Locate every Plasmodium falciparum-infected red blood cell.
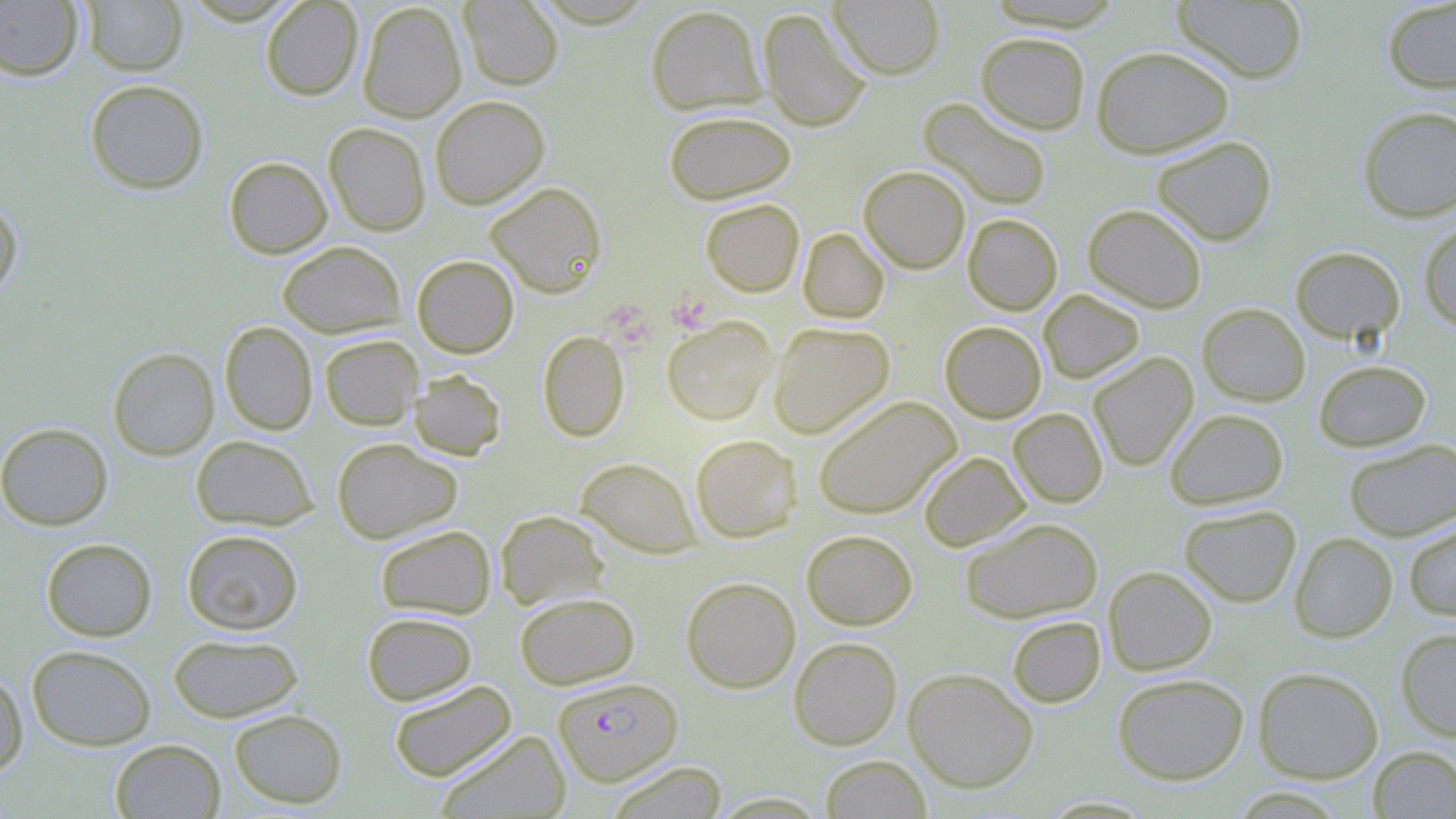
Approximate bounding boxes as (x1, y1, x2, y2) in pixels.
Plasmodium falciparum-infected red blood cells: (552, 677, 683, 786).

slide-level diagnosis = Plasmodium falciparum
preparation = thin blood film
magnification = 1000x
modality = light microscopy
stain = May-Grünwald-Giemsa
field of view = one of a larger specimen
platelet locations = approximate bounding boxes as (x1, y1, x2, y2) in pixels: (670, 296, 712, 336), (599, 302, 657, 363)
image size = 1456×819 pixels
uninfected red blood cell locations = approximate bounding boxes as (x1, y1, x2, y2) in pixels: (80, 0, 187, 75), (260, 0, 364, 101), (458, 0, 564, 90), (828, 0, 946, 80), (1172, 0, 1309, 83), (0, 1, 83, 80), (1381, 1, 1456, 93), (357, 2, 467, 122), (645, 4, 766, 115), (757, 7, 870, 132), (975, 32, 1091, 134), (1091, 45, 1234, 158), (84, 79, 209, 194), (429, 95, 550, 209), (918, 97, 1053, 210), (1357, 105, 1456, 222), (664, 110, 796, 205), (324, 122, 431, 236), (1151, 135, 1277, 245), (223, 156, 332, 258), (859, 166, 971, 273), (484, 181, 607, 298), (0, 197, 23, 298), (700, 198, 804, 297), (1082, 203, 1207, 313), (963, 213, 1063, 315), (1418, 219, 1456, 332), (798, 228, 889, 324), (277, 241, 406, 338), (1290, 246, 1405, 344), (412, 254, 519, 358), (1038, 289, 1144, 384), (1197, 303, 1310, 406), (662, 316, 776, 425), (219, 321, 318, 435), (939, 321, 1047, 423), (769, 322, 895, 438), (537, 330, 630, 442), (319, 334, 423, 430), (107, 347, 219, 460), (1087, 352, 1199, 471), (1313, 359, 1431, 452), (408, 369, 507, 461), (812, 395, 960, 519), (1009, 408, 1108, 508), (1164, 408, 1290, 509), (0, 422, 113, 531), (190, 434, 318, 530), (690, 434, 802, 542), (331, 437, 462, 544), (1343, 438, 1456, 541), (918, 451, 1031, 552), (575, 457, 700, 558), (1178, 504, 1301, 607), (495, 509, 611, 610), (960, 516, 1103, 623), (1403, 518, 1456, 622), (374, 524, 496, 620), (182, 529, 304, 635), (802, 529, 918, 630), (1289, 532, 1397, 643), (41, 538, 157, 642), (1103, 565, 1218, 675), (681, 576, 801, 693), (515, 591, 640, 690), (361, 611, 477, 706), (1007, 616, 1105, 707), (1396, 627, 1456, 741), (168, 633, 303, 723), (788, 637, 902, 750), (27, 644, 157, 750), (1252, 666, 1384, 783), (903, 668, 1039, 793), (0, 670, 28, 778), (1112, 673, 1249, 784), (388, 678, 517, 783), (228, 708, 347, 809), (435, 730, 571, 818), (110, 738, 226, 818), (1369, 746, 1456, 818), (819, 755, 932, 818), (605, 761, 728, 817), (708, 792, 830, 818)